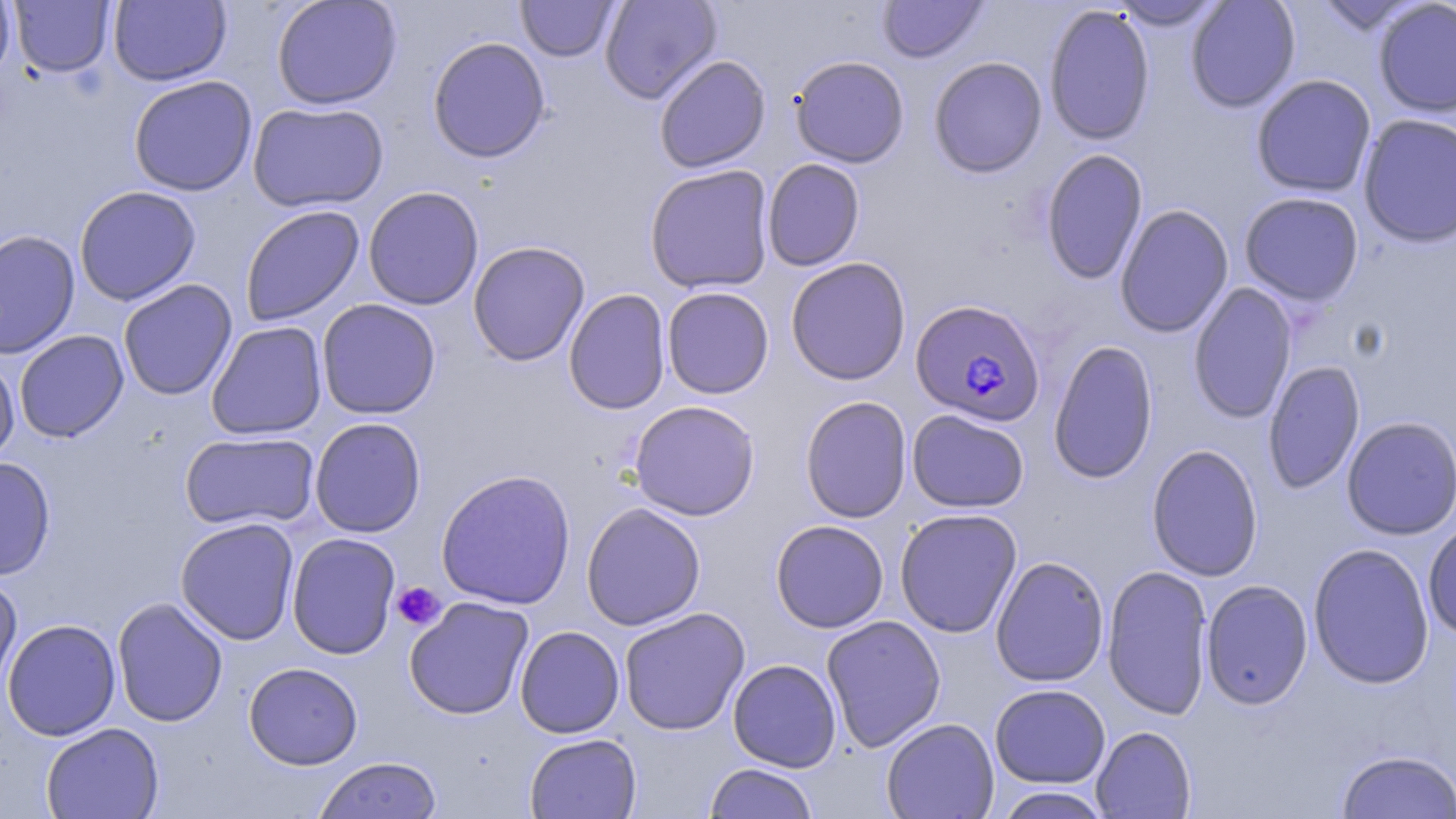
slide_level_diagnosis: Plasmodium falciparum
modality: light microscopy
stain: May-Grünwald-Giemsa
field_of_view: single
platelet_locations: 'approximate bounding boxes as (x1,y1)-(x2,y2) corner pairs in pixels: (391,581)-(446,631)'
magnification: 1000x
uninfected_red_blood_cell_locations: 'approximate bounding boxes as (x1,y1)-(x2,y2) corner pairs in pixels: (0,0)-(16,86), (9,0)-(115,77), (109,0)-(232,86), (271,0)-(402,110), (516,0)-(619,62), (600,0)-(722,104), (877,0)-(988,63), (1185,0)-(1301,113), (1373,0)-(1456,118), (1108,1)-(1227,30), (1314,1)-(1425,36), (1044,4)-(1155,145), (427,36)-(551,163), (653,54)-(771,173), (789,55)-(910,167), (928,56)-(1048,178), (1251,74)-(1377,197), (128,75)-(258,196), (248,101)-(389,213), (1358,112)-(1456,248), (1040,148)-(1148,284), (762,158)-(865,271), (644,164)-(775,294), (74,186)-(201,305), (363,186)-(484,310), (1239,192)-(1364,306), (1115,204)-(1234,338), (240,205)-(365,327), (0,229)-(80,359), (468,241)-(590,366), (785,256)-(911,385), (118,279)-(238,401), (1187,282)-(1297,424), (661,286)-(774,399), (563,288)-(671,414), (316,299)-(441,419), (206,321)-(328,441), (14,330)-(129,443), (1048,340)-(1158,484), (0,353)-(20,466), (1262,360)-(1366,495), (800,395)-(912,523), (629,400)-(760,521), (907,409)-(1029,513), (1341,415)-(1456,540), (309,417)-(427,538), (180,431)-(320,530), (1146,444)-(1264,581), (0,456)-(55,581), (436,469)-(576,610), (581,502)-(706,631), (895,508)-(1022,638), (175,517)-(300,645), (770,519)-(889,633), (1422,519)-(1456,641), (286,532)-(400,659), (1308,543)-(1435,689), (990,555)-(1110,687), (1102,564)-(1213,719), (0,573)-(22,698), (1200,579)-(1313,709), (112,596)-(228,727), (403,596)-(534,720), (618,607)-(750,735), (821,615)-(946,752), (2,618)-(121,741), (514,625)-(625,738), (727,658)-(841,772), (244,662)-(363,769), (989,684)-(1111,787), (881,717)-(999,819), (40,722)-(164,819), (1090,726)-(1196,818), (524,733)-(642,818), (1336,749)-(1456,819), (313,756)-(442,819), (704,762)-(818,819), (994,786)-(1112,818)'
image_size: 1456×819 pixels
preparation: thin blood film
plasmodium_falciparum_infected_red_blood_cell_locations: 'approximate bounding boxes as (x1,y1)-(x2,y2) corner pairs in pixels: (910,298)-(1046,427)'